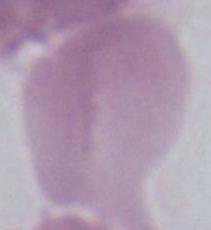
{
  "identification": "erythrocyte",
  "modality": "micrograph",
  "magnification": "1000x"
}